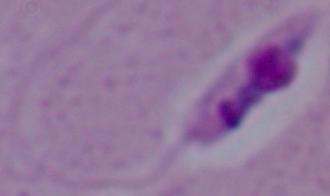

1000x magnification. Micrograph. A Leishmania parasite is seen.